State which cell type is depicted.
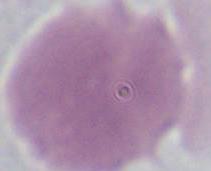

This is an erythrocyte.

Summary:
  - Magnification: 1000x
  - Modality: photomicrograph